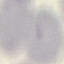

malaria_status: uninfected
stain: Giemsa
preparation: thin blood smear
image_type: automatically extracted cell patch, resized to 64 × 64 pixels
capture: smartphone camera at the microscope eyepiece